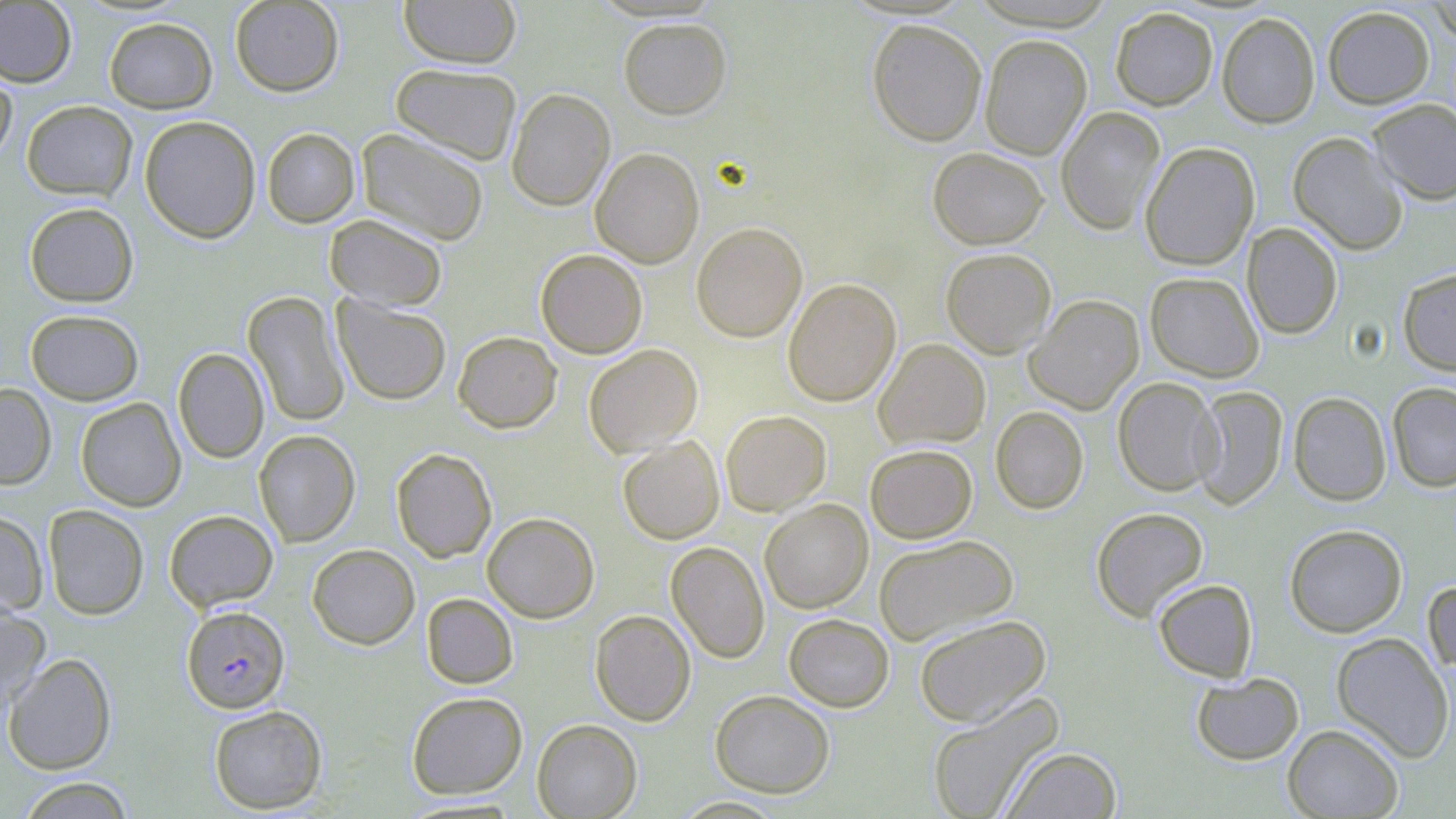
Approximate bounding boxes as [x1, y1, x2, y2] in pixels. Plasmodium falciparum-infected red blood cell locations: [181, 605, 290, 713]. Uninfected red blood cell locations: [229, 0, 344, 96], [399, 0, 521, 68], [1428, 0, 1456, 43], [0, 1, 76, 87], [1110, 6, 1218, 110], [1322, 6, 1434, 109], [1217, 12, 1320, 128], [104, 17, 217, 113], [618, 18, 731, 119], [867, 19, 987, 146], [980, 34, 1092, 159], [390, 63, 522, 165], [0, 65, 17, 168], [506, 87, 615, 211], [1367, 98, 1456, 204], [22, 100, 137, 201], [1056, 106, 1165, 234], [139, 115, 261, 243], [262, 127, 360, 228], [357, 129, 489, 246], [1288, 132, 1408, 255], [1139, 141, 1259, 271], [590, 147, 705, 268], [927, 147, 1048, 249], [24, 202, 139, 307], [325, 214, 448, 311], [691, 222, 807, 342], [1243, 223, 1343, 340], [940, 248, 1057, 358], [535, 249, 648, 358], [1398, 268, 1456, 375], [1145, 272, 1264, 382], [783, 278, 901, 406], [243, 290, 350, 428], [332, 295, 451, 406], [1025, 295, 1144, 414], [25, 309, 144, 405], [453, 331, 562, 433], [874, 339, 990, 450], [584, 344, 703, 456], [173, 348, 269, 463], [1112, 377, 1222, 496], [1387, 382, 1456, 492], [0, 383, 56, 490], [1191, 386, 1288, 510], [1288, 391, 1391, 506], [76, 397, 186, 511], [990, 406, 1089, 514], [720, 410, 831, 516], [253, 430, 361, 547], [617, 436, 724, 544], [864, 444, 977, 543], [391, 448, 496, 562], [759, 499, 873, 613], [43, 504, 150, 620], [1091, 506, 1209, 621], [164, 509, 278, 612], [0, 511, 48, 616], [482, 512, 599, 622], [1284, 524, 1407, 637], [874, 534, 1018, 645], [666, 541, 770, 663], [307, 544, 420, 649], [1423, 578, 1456, 681], [1153, 579, 1258, 682], [421, 593, 518, 689], [0, 605, 51, 718], [590, 609, 695, 726], [784, 613, 894, 712], [914, 614, 1051, 727], [1331, 632, 1454, 763], [3, 652, 117, 774], [1191, 672, 1304, 765], [710, 689, 835, 797], [406, 691, 528, 798], [926, 693, 1064, 819], [209, 705, 327, 814], [532, 719, 642, 818], [1282, 724, 1404, 818], [1001, 746, 1122, 819], [15, 776, 136, 818], [670, 796, 789, 818]. Slide-level diagnosis: Plasmodium falciparum. 1000x magnification. Thin blood smear. May-Grünwald-Giemsa-stained preparation. Image is 1456×819 pixels. Optical microscopy. One field of a larger specimen.